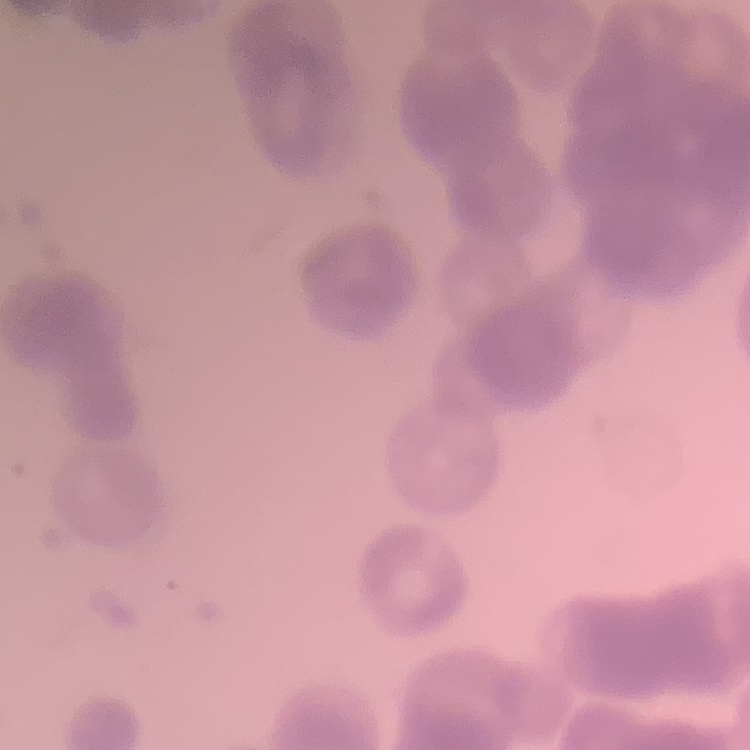
Summary:
  - Red blood cell morphology: rouleaux formation
  - Stain: Field's or Giemsa
  - Preparation: thin peripheral smear
  - Image type: one tile cut from a larger photomicrograph